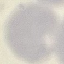

{
  "malaria_status": "uninfected",
  "stain": "Giemsa",
  "preparation": "thin blood film",
  "image_type": "automatically extracted cell patch, resized to 64 × 64 pixels",
  "capture": "smartphone through the microscope eyepiece"
}